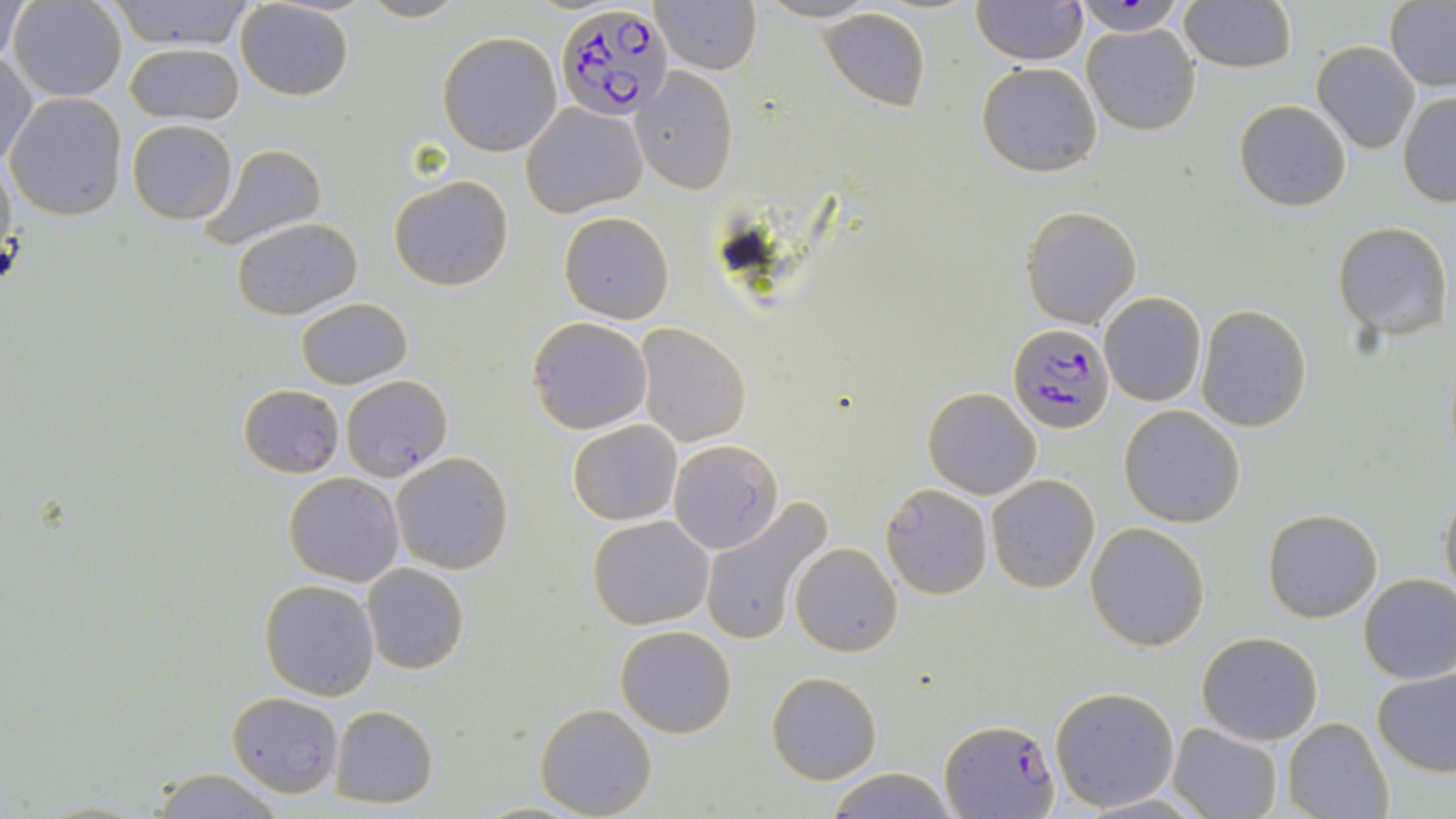

Summary:
  - Coordinate format: approximate bounding boxes as [x1, y1, x2, y2] in pixels
  - Plasmodium falciparum-infected red blood cell locations: [556, 4, 675, 121], [1007, 324, 1113, 432], [942, 716, 1059, 819]
  - Uninfected red blood cell locations: [2, 0, 30, 67], [8, 0, 127, 102], [105, 0, 255, 50], [359, 0, 468, 23], [755, 0, 879, 24], [971, 0, 1088, 67], [236, 1, 354, 101], [1071, 1, 1188, 35], [1178, 1, 1296, 72], [652, 2, 761, 76], [1385, 2, 1456, 89], [818, 7, 931, 112], [1081, 23, 1200, 135], [438, 31, 564, 156], [124, 40, 245, 125], [1312, 40, 1421, 154], [0, 52, 39, 168], [975, 61, 1102, 176], [632, 68, 739, 194], [1397, 91, 1456, 206], [5, 92, 127, 222], [1234, 99, 1351, 211], [522, 101, 648, 217], [127, 119, 239, 224], [199, 142, 329, 251], [0, 154, 17, 268], [389, 175, 513, 291], [1021, 206, 1141, 329], [558, 212, 673, 322], [231, 216, 363, 320], [1332, 221, 1452, 340], [1099, 293, 1206, 407], [295, 297, 412, 389], [1195, 306, 1312, 432], [527, 317, 652, 434], [635, 323, 751, 447], [340, 374, 451, 481], [239, 384, 344, 477], [922, 386, 1041, 498], [1120, 405, 1245, 528], [568, 420, 682, 525], [665, 438, 785, 557], [389, 452, 514, 574], [283, 472, 405, 587], [987, 475, 1099, 593], [881, 482, 993, 600], [1438, 489, 1456, 602], [700, 496, 833, 648], [1262, 507, 1382, 622], [588, 515, 715, 629], [1085, 521, 1211, 650], [790, 542, 902, 657], [362, 563, 469, 675], [1358, 573, 1456, 684], [259, 579, 380, 700], [615, 625, 737, 739], [1196, 631, 1323, 745], [1371, 666, 1456, 778], [767, 672, 881, 784], [1049, 687, 1180, 812], [226, 690, 342, 797], [535, 702, 657, 818], [330, 705, 438, 808], [1282, 718, 1395, 819], [1167, 722, 1282, 819], [824, 767, 958, 819], [147, 768, 288, 819]
  - Slide-level diagnosis: Plasmodium falciparum
  - Modality: optical microscopy
  - Image size: 1456×819 pixels
  - Field of view: single
  - Magnification: 1000x
  - Preparation: thin blood smear
  - Stain: May-Grünwald-Giemsa